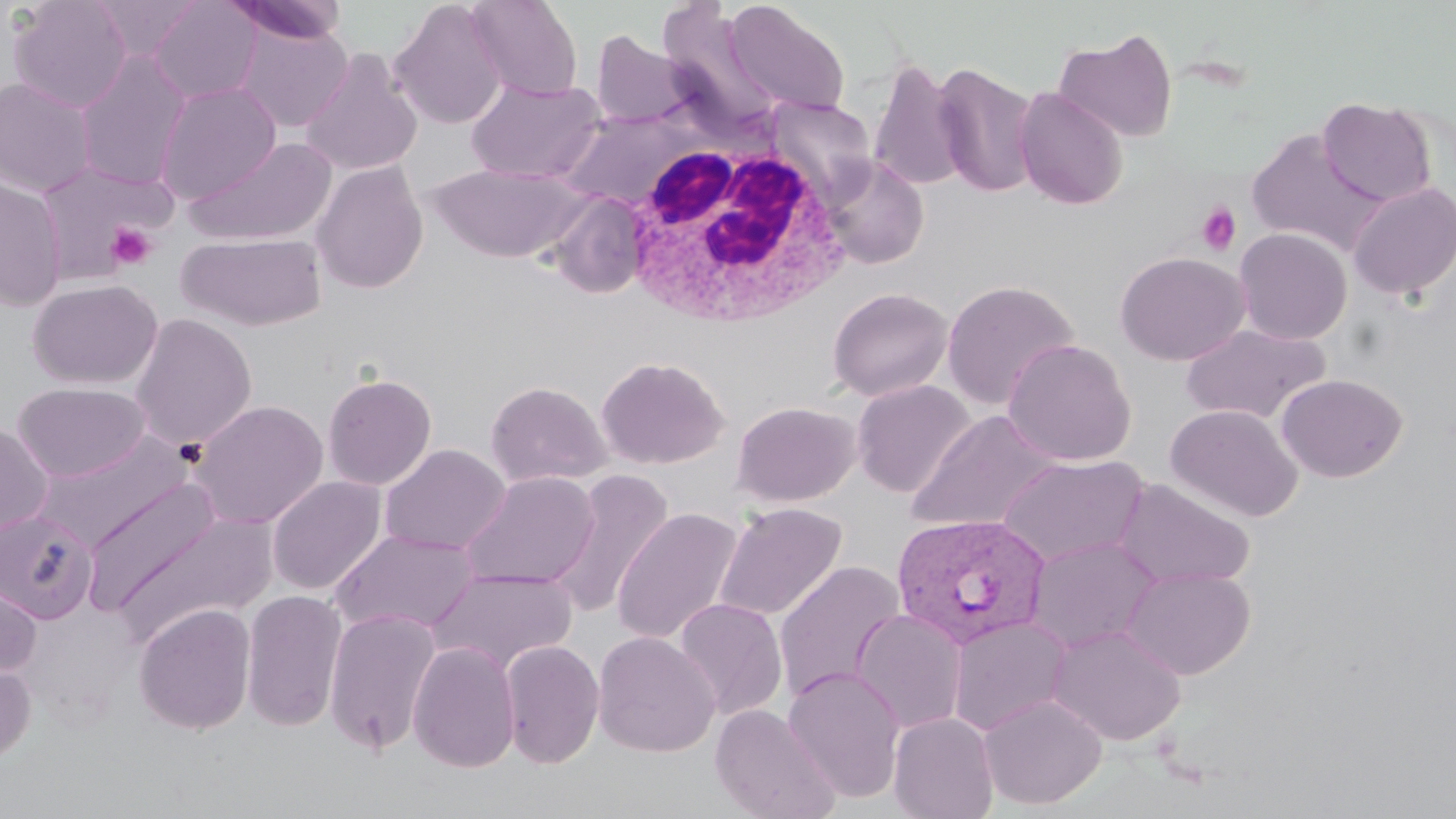
Summary:
  - Coordinate format: approximate bounding boxes as named x1/y1/x2/y2 corners in pixels
  - Uninfected red blood cell locations: (x1=9, y1=0, x2=133, y2=113), (x1=90, y1=0, x2=203, y2=61), (x1=149, y1=0, x2=262, y2=104), (x1=224, y1=0, x2=348, y2=45), (x1=388, y1=0, x2=507, y2=129), (x1=467, y1=0, x2=584, y2=100), (x1=657, y1=0, x2=778, y2=133), (x1=723, y1=1, x2=851, y2=116), (x1=236, y1=23, x2=353, y2=132), (x1=1054, y1=28, x2=1178, y2=143), (x1=590, y1=30, x2=690, y2=129), (x1=75, y1=50, x2=193, y2=191), (x1=300, y1=50, x2=423, y2=177), (x1=868, y1=58, x2=968, y2=193), (x1=932, y1=60, x2=1041, y2=200), (x1=0, y1=77, x2=97, y2=197), (x1=466, y1=78, x2=606, y2=184), (x1=154, y1=81, x2=282, y2=204), (x1=1014, y1=87, x2=1128, y2=210), (x1=1318, y1=97, x2=1436, y2=206), (x1=558, y1=110, x2=693, y2=208), (x1=1245, y1=129, x2=1386, y2=255), (x1=184, y1=136, x2=338, y2=247), (x1=821, y1=155, x2=929, y2=269), (x1=311, y1=161, x2=429, y2=294), (x1=35, y1=162, x2=172, y2=279), (x1=428, y1=164, x2=590, y2=262), (x1=0, y1=176, x2=68, y2=311), (x1=1347, y1=181, x2=1456, y2=301), (x1=547, y1=191, x2=651, y2=299), (x1=1233, y1=227, x2=1353, y2=345), (x1=176, y1=232, x2=327, y2=331), (x1=1115, y1=251, x2=1250, y2=365), (x1=26, y1=278, x2=163, y2=390), (x1=941, y1=279, x2=1081, y2=411), (x1=828, y1=287, x2=953, y2=402), (x1=129, y1=313, x2=258, y2=452), (x1=1180, y1=322, x2=1331, y2=425), (x1=1002, y1=338, x2=1137, y2=466), (x1=596, y1=355, x2=729, y2=470), (x1=322, y1=372, x2=437, y2=490), (x1=1277, y1=373, x2=1408, y2=482), (x1=851, y1=379, x2=976, y2=498), (x1=485, y1=380, x2=611, y2=488), (x1=13, y1=381, x2=151, y2=483), (x1=190, y1=399, x2=329, y2=529), (x1=731, y1=400, x2=861, y2=507), (x1=1166, y1=404, x2=1303, y2=522), (x1=907, y1=410, x2=1062, y2=533), (x1=0, y1=422, x2=54, y2=538), (x1=34, y1=432, x2=194, y2=549), (x1=379, y1=444, x2=511, y2=556), (x1=996, y1=455, x2=1150, y2=568), (x1=547, y1=469, x2=674, y2=621), (x1=460, y1=471, x2=600, y2=591), (x1=267, y1=475, x2=387, y2=596), (x1=80, y1=477, x2=225, y2=615), (x1=262, y1=477, x2=375, y2=730), (x1=1115, y1=478, x2=1256, y2=589), (x1=714, y1=502, x2=847, y2=622), (x1=611, y1=507, x2=745, y2=646), (x1=0, y1=510, x2=98, y2=623), (x1=110, y1=511, x2=280, y2=643), (x1=329, y1=529, x2=482, y2=636), (x1=1025, y1=535, x2=1163, y2=653), (x1=773, y1=560, x2=907, y2=704), (x1=1122, y1=565, x2=1256, y2=679), (x1=429, y1=567, x2=578, y2=675), (x1=0, y1=574, x2=42, y2=679), (x1=240, y1=590, x2=348, y2=732), (x1=674, y1=598, x2=788, y2=720), (x1=134, y1=603, x2=256, y2=734), (x1=322, y1=607, x2=442, y2=755), (x1=850, y1=608, x2=968, y2=735), (x1=947, y1=616, x2=1073, y2=736), (x1=1046, y1=622, x2=1186, y2=746), (x1=592, y1=631, x2=721, y2=757), (x1=500, y1=639, x2=605, y2=768), (x1=407, y1=641, x2=520, y2=773), (x1=0, y1=657, x2=36, y2=765), (x1=782, y1=665, x2=906, y2=802), (x1=978, y1=693, x2=1108, y2=810), (x1=710, y1=703, x2=841, y2=819), (x1=889, y1=712, x2=999, y2=819)
  - Plasmodium vivax-infected red blood cell locations: (x1=890, y1=513, x2=1051, y2=650)
  - Platelet locations: (x1=1196, y1=201, x2=1242, y2=256), (x1=105, y1=222, x2=158, y2=271)
  - White blood cell locations: (x1=621, y1=136, x2=853, y2=326)
  - Slide-level diagnosis: Plasmodium vivax
  - Field of view: single
  - Magnification: 1000x
  - Preparation: thin blood film
  - Stain: May-Grünwald-Giemsa
  - Image size: 1456×819 pixels
  - Modality: light microscopy